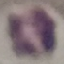

Result: negative for malaria parasites. Thin blood smear. Acquired by smartphone through the microscope eyepiece. Automatically extracted cell patch, resized to 64 × 64 pixels. Giemsa stain.